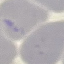

Summary:
  - Malaria status: uninfected
  - Image type: cell patch, automatically extracted from a larger field of view and resized to 64 × 64 pixels
  - Preparation: thin blood film
  - Capture: smartphone camera at the microscope eyepiece
  - Stain: Giemsa